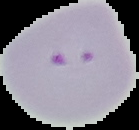 Image is 139×130 pixels. Malaria status: parasitized. From a thin blood smear. Cell region segmented out of the field of view; the surrounding area is masked to black.